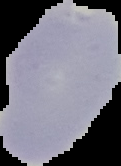

Summary:
  - Preparation: thin blood film
  - Result: malaria parasites detected
  - Image size: 121×166 pixels
  - Image type: cell region segmented out of the field of view; surrounding area masked to black